Comment on the morphology of the red blood cells.
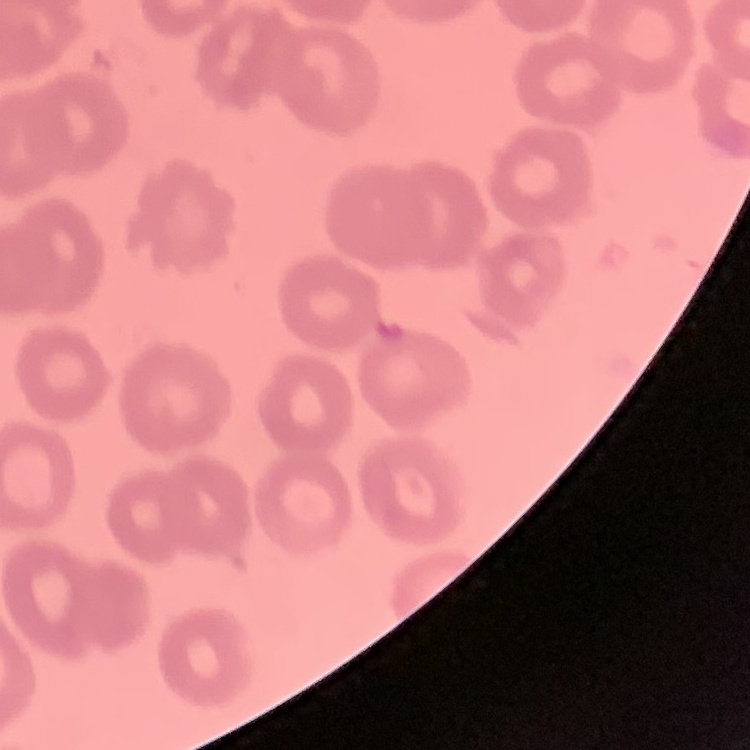

They show no rouleaux formation.

Summary:
  - Stain: Field's or Giemsa
  - Image type: one tile cut from a larger photomicrograph
  - Preparation: thin blood film